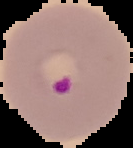
From a thin blood film. Result: malaria parasites identified. The area outside the segmented cell region is set to black. Image is 133×148 pixels.